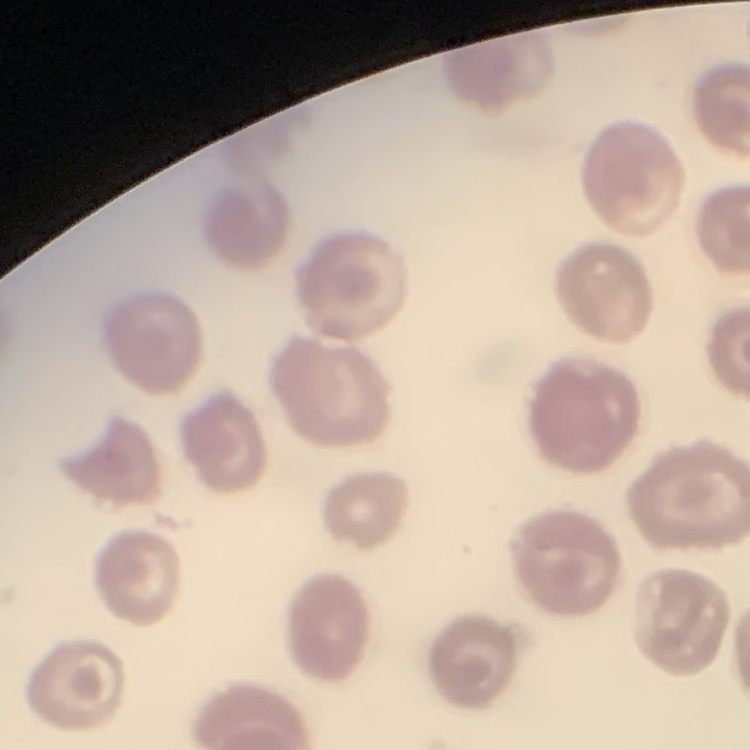
Summary:
  - Erythrocyte morphology: no rouleaux formation
  - Preparation: thin peripheral smear
  - Stain: Field's or Giemsa
  - Image type: one tile cut from a larger photomicrograph